Describe the morphology of the red blood cells.
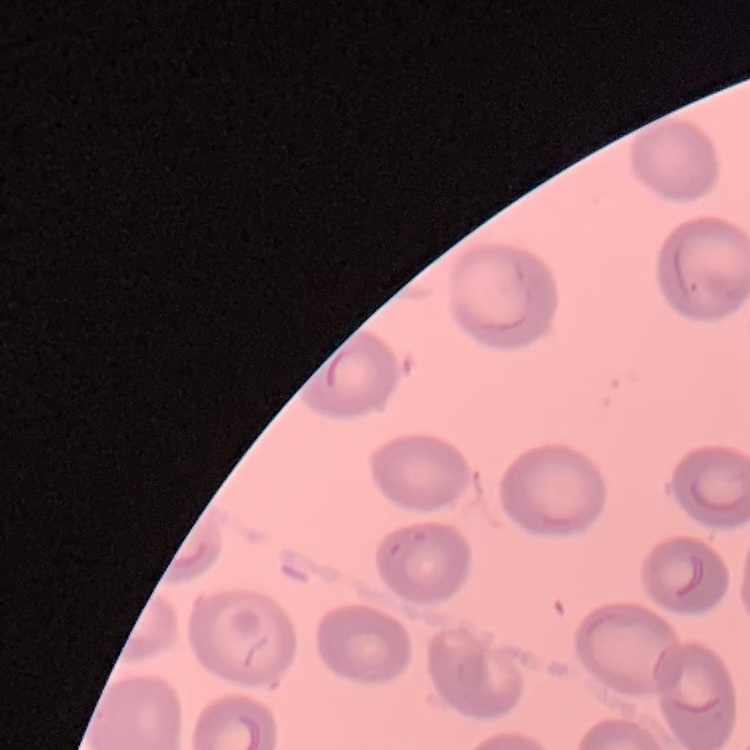
They show no rouleaux formation.

stain: Field's or Giemsa
preparation: thin peripheral smear
image_type: square crop of a larger photomicrograph